Comment on the morphology of the erythrocytes.
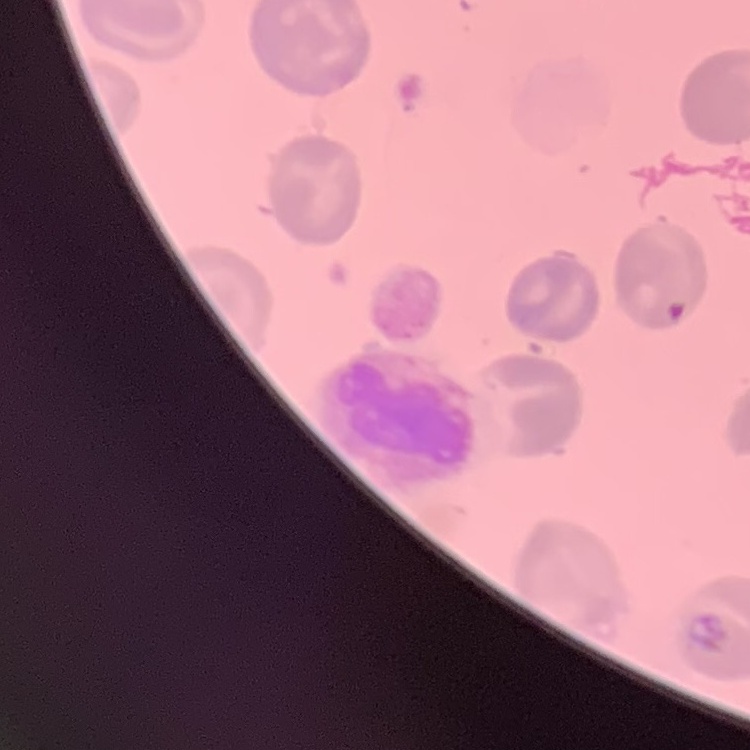
They show no rouleaux formation.

Summary:
  - Stain: Field's or Giemsa
  - Image type: square crop of a larger photomicrograph
  - Preparation: thin blood smear